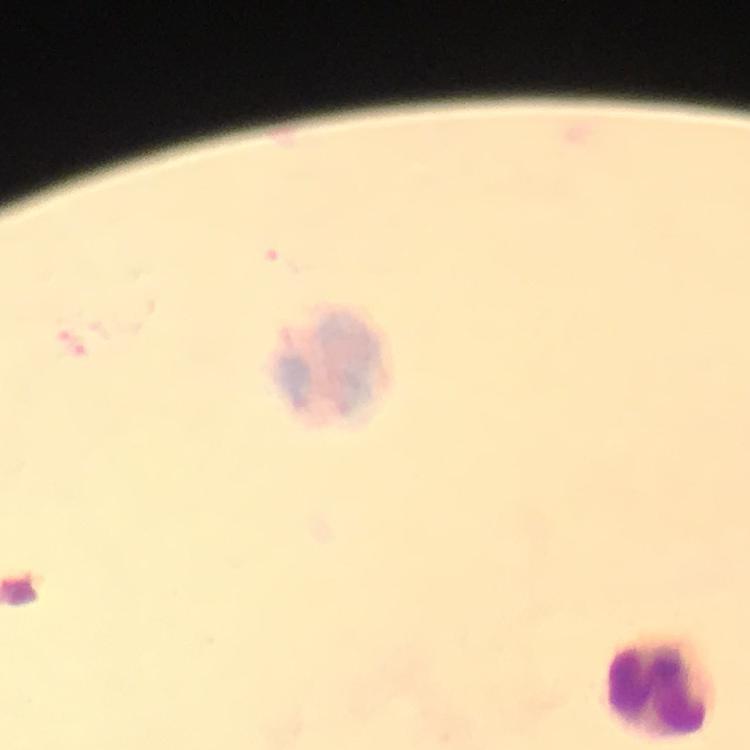
Approximate centers as [x, y] in pixels.
Summary:
  - Leukocyte locations: [334, 365], [662, 687]
  - Malaria parasites: none seen
  - Image size: 750×750 pixels
  - Magnification: 100x
  - Immersion oil: applied
  - Preparation: thick smear
  - Cropped from: a single field of view
  - Stain: Giemsa
  - Capture: smartphone camera through the microscope
  - Context: from a diagnostic examination for malaria